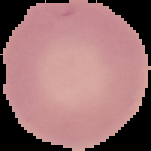
Summary:
  - Preparation: thin blood film
  - Image size: 151×151 pixels
  - Result: no Plasmodium parasites detected
  - Image type: segmented cell region on a black background